Give the position of every malaria parasite.
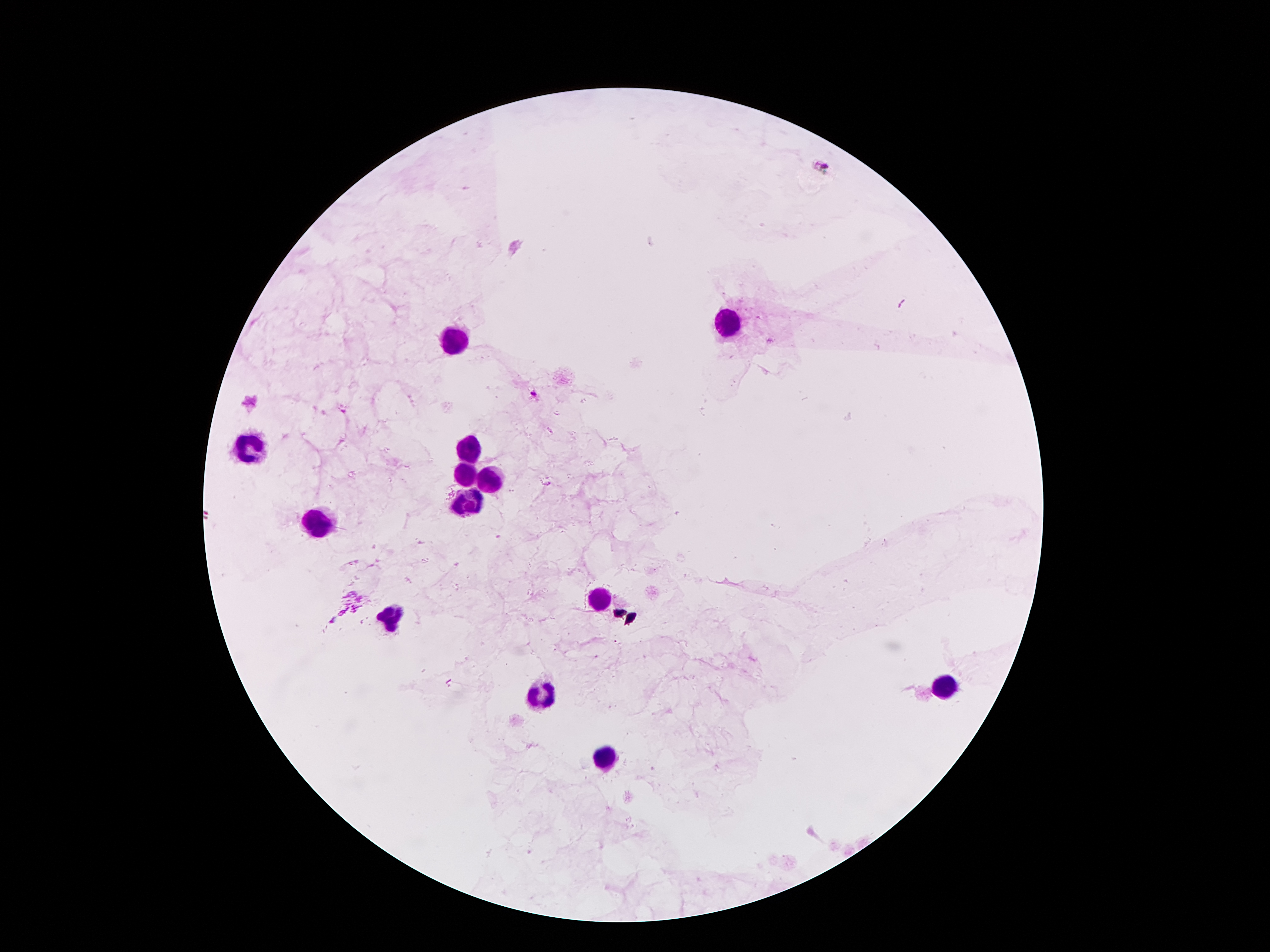
Approximate object centers, in pixels from the top-left corner.
Malaria parasites: (x=821, y=165), (x=531, y=394).

Leukocyte locations: (x=731, y=328), (x=456, y=341), (x=251, y=447), (x=467, y=449), (x=465, y=469), (x=485, y=483), (x=467, y=496), (x=319, y=525), (x=602, y=600), (x=394, y=615), (x=945, y=688), (x=540, y=697), (x=607, y=755). Photographed through the microscope eyepiece with a smartphone camera. Image is 1270×952 pixels. Giemsa-stained preparation. 100x magnification. Thick blood smear. Patient malaria status: infected with Plasmodium falciparum. Single field of view.